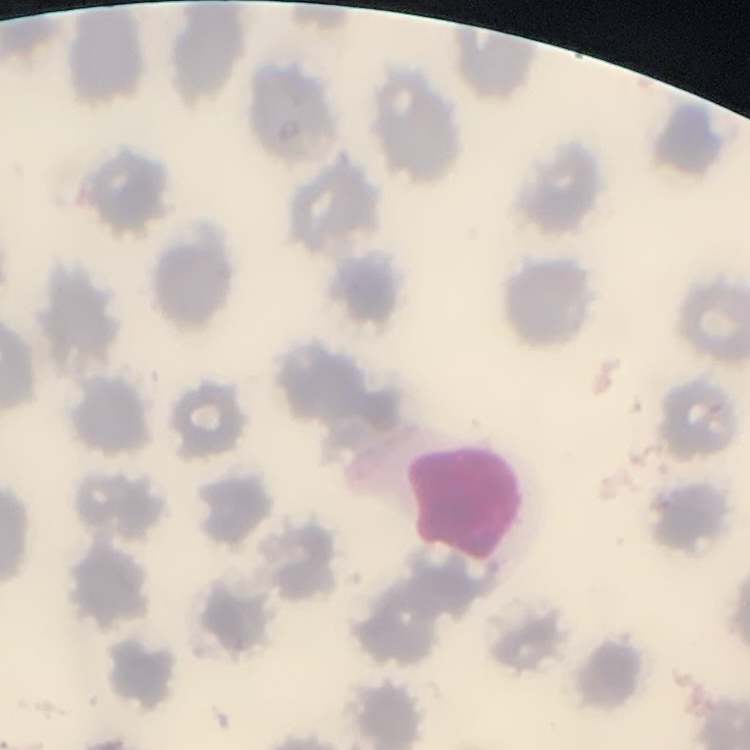

Summary:
  - Red blood cell morphology: no rouleaux formation
  - Stain: Field's or Giemsa
  - Image type: square crop of a larger photomicrograph
  - Preparation: thin blood smear